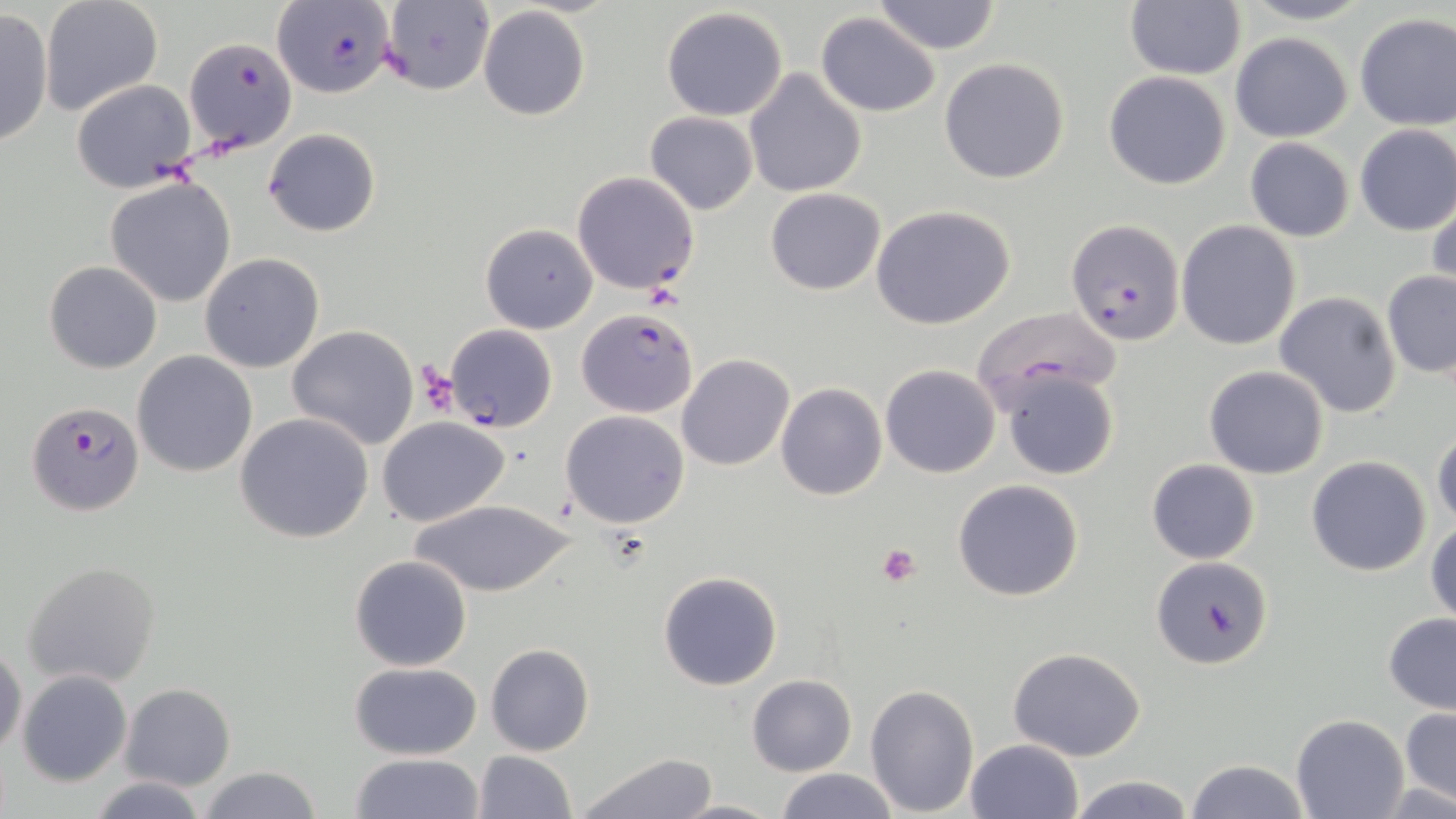
Approximate bounding boxes as (x1,y1)-(x2,y2) corner pairs in pixels. Plasmodium falciparum-infected red blood cell locations: (272,2)-(392,99), (184,38)-(295,153), (1067,218)-(1185,347), (576,307)-(697,418), (446,324)-(557,432), (28,401)-(145,515), (1150,557)-(1274,669). Uninfected red blood cell locations: (872,0)-(1003,54), (1234,0)-(1377,27), (39,1)-(163,116), (379,1)-(495,97), (1123,2)-(1246,80), (476,6)-(590,123), (0,7)-(53,149), (660,7)-(789,122), (815,13)-(941,117), (1353,13)-(1456,129), (1230,32)-(1354,142), (938,57)-(1069,184), (743,69)-(867,198), (1102,71)-(1232,190), (71,79)-(198,191), (645,111)-(758,214), (1353,123)-(1456,235), (264,128)-(380,237), (1244,138)-(1355,242), (572,170)-(701,294), (105,178)-(237,306), (765,188)-(885,295), (1427,193)-(1456,301), (872,203)-(1018,332), (1176,220)-(1302,351), (479,222)-(597,333), (199,252)-(325,373), (44,260)-(162,373), (1382,269)-(1456,379), (1273,291)-(1404,417), (971,304)-(1122,409), (287,324)-(420,450), (132,350)-(257,477), (677,354)-(796,472), (880,364)-(1001,479), (1204,365)-(1330,480), (999,367)-(1119,480), (775,382)-(887,501), (559,410)-(690,529), (234,412)-(374,544), (376,416)-(509,527), (1431,426)-(1455,531), (1305,455)-(1432,576), (1147,459)-(1259,565), (953,478)-(1085,601), (409,499)-(574,598), (1426,517)-(1456,626), (350,555)-(473,671), (22,561)-(162,688), (658,570)-(784,691), (1383,613)-(1455,713), (0,641)-(26,757), (485,643)-(595,756), (1007,645)-(1147,762), (351,662)-(481,759), (18,670)-(132,787), (747,674)-(856,776), (119,683)-(236,790), (864,684)-(979,814), (1399,706)-(1455,813), (1291,714)-(1409,819), (965,738)-(1086,819), (471,751)-(577,819), (351,752)-(483,819), (572,752)-(721,819), (1185,759)-(1311,819), (196,765)-(326,819), (775,768)-(898,819), (1067,773)-(1196,818), (86,775)-(211,819), (673,795)-(778,817). Platelet locations: (416,363)-(461,413), (877,543)-(923,588). Slide-level diagnosis: Plasmodium falciparum. Captured at 1000x magnification. Thin blood film. Image is 1456×819 pixels. May-Grünwald-Giemsa stain. Optical microscopy. One field of a larger specimen.